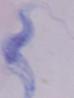
{
  "modality": "micrograph",
  "magnification": "1000x",
  "identification": "trypanosome"
}